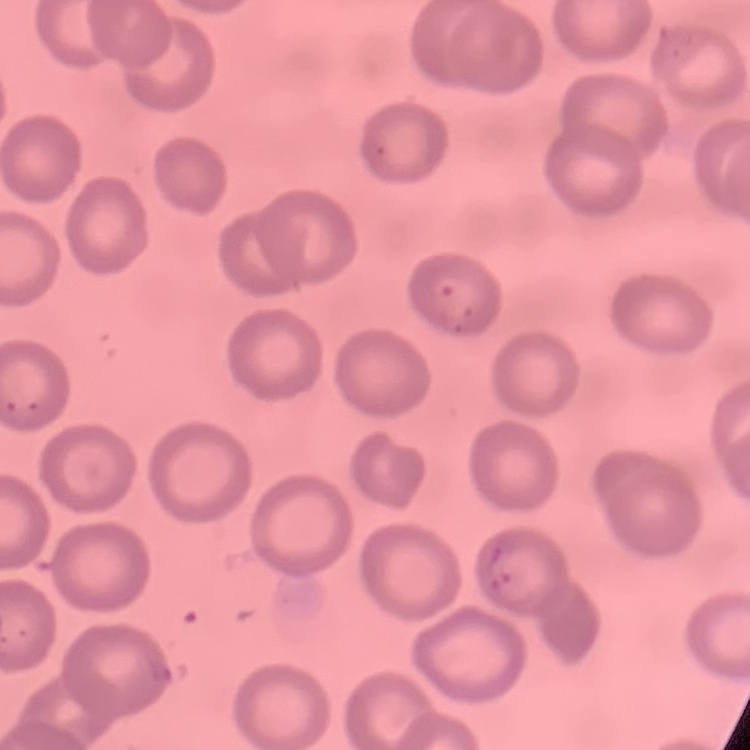 The red blood cells exhibit no rouleaux formation. Thin blood smear. Square crop of a larger photomicrograph. Field's or Giemsa stain.